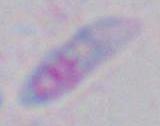

magnification = 1000x
modality = photomicrograph
identification = Toxoplasma gondii